Name the parasite shown.
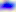

Toxoplasma gondii.

{
  "modality": "micrograph",
  "magnification": "400x"
}